Identify the cell.
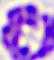
A leukocyte.

Summary:
  - Modality: micrograph
  - Magnification: 400x